State which parasite is depicted.
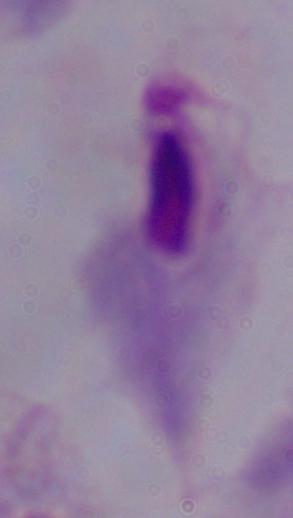
This is a trichomonad.

Micrograph. Captured at 1000x magnification.